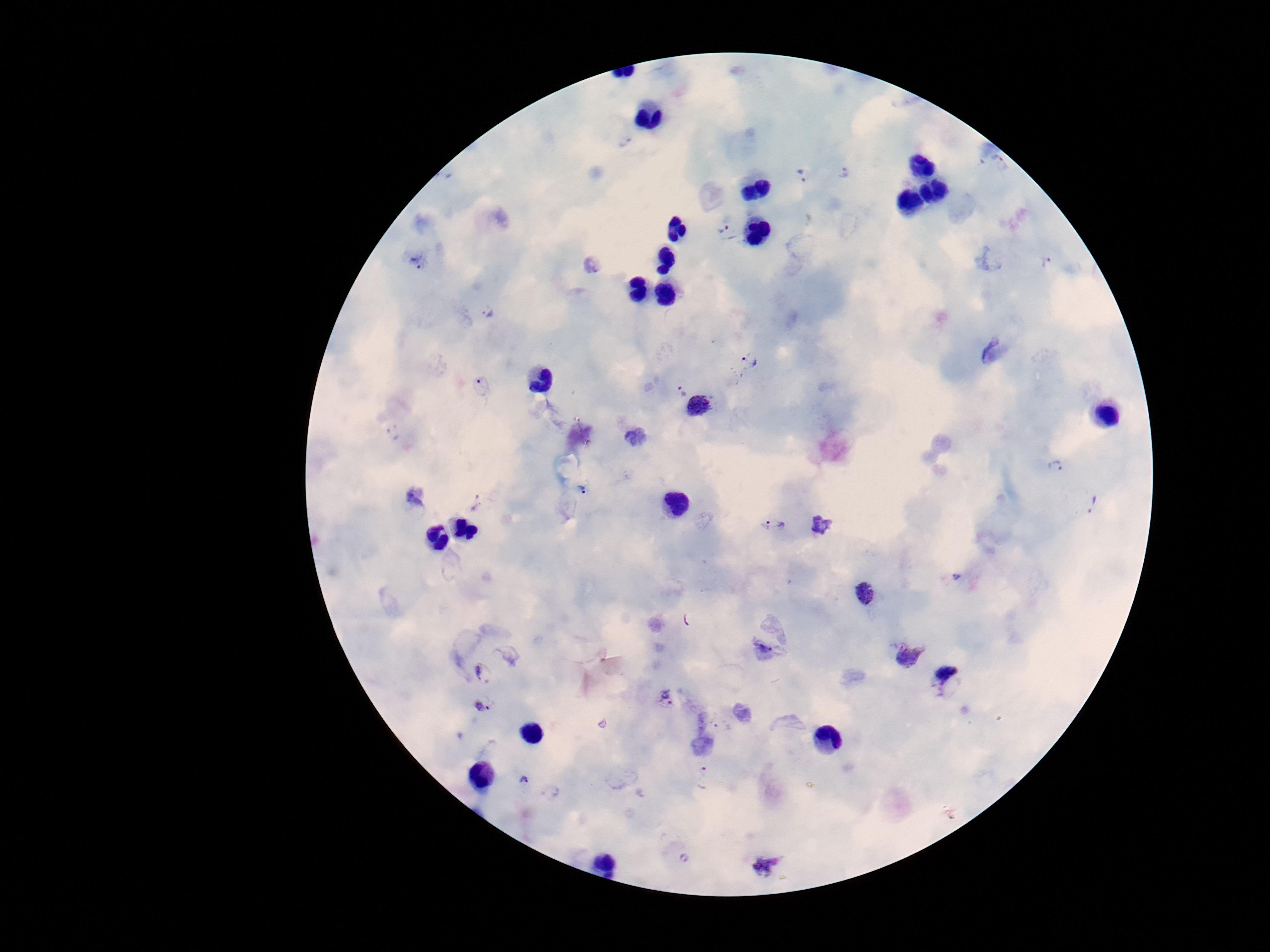
Approximate object centers, in pixels from the top-left corner.
Summary:
  - Plasmodium parasite locations: (x=846, y=174), (x=802, y=177), (x=723, y=226), (x=420, y=260), (x=1048, y=261), (x=487, y=312), (x=992, y=353), (x=749, y=359), (x=483, y=386), (x=682, y=391), (x=699, y=406), (x=1056, y=466), (x=582, y=488), (x=477, y=503), (x=1094, y=504), (x=773, y=527), (x=958, y=577), (x=865, y=595), (x=688, y=620), (x=768, y=642), (x=907, y=656), (x=482, y=673), (x=947, y=682), (x=666, y=698), (x=483, y=706), (x=704, y=775), (x=523, y=780), (x=551, y=790), (x=686, y=856), (x=765, y=865)
  - Patient malaria status: infected
  - Magnification: 100x
  - Capture: smartphone camera through the microscope eyepiece
  - Preparation: thick peripheral-blood smear
  - Stain: Giemsa
  - Image size: 1270×952 pixels
  - Field of view: single